Locate every Plasmodium parasite.
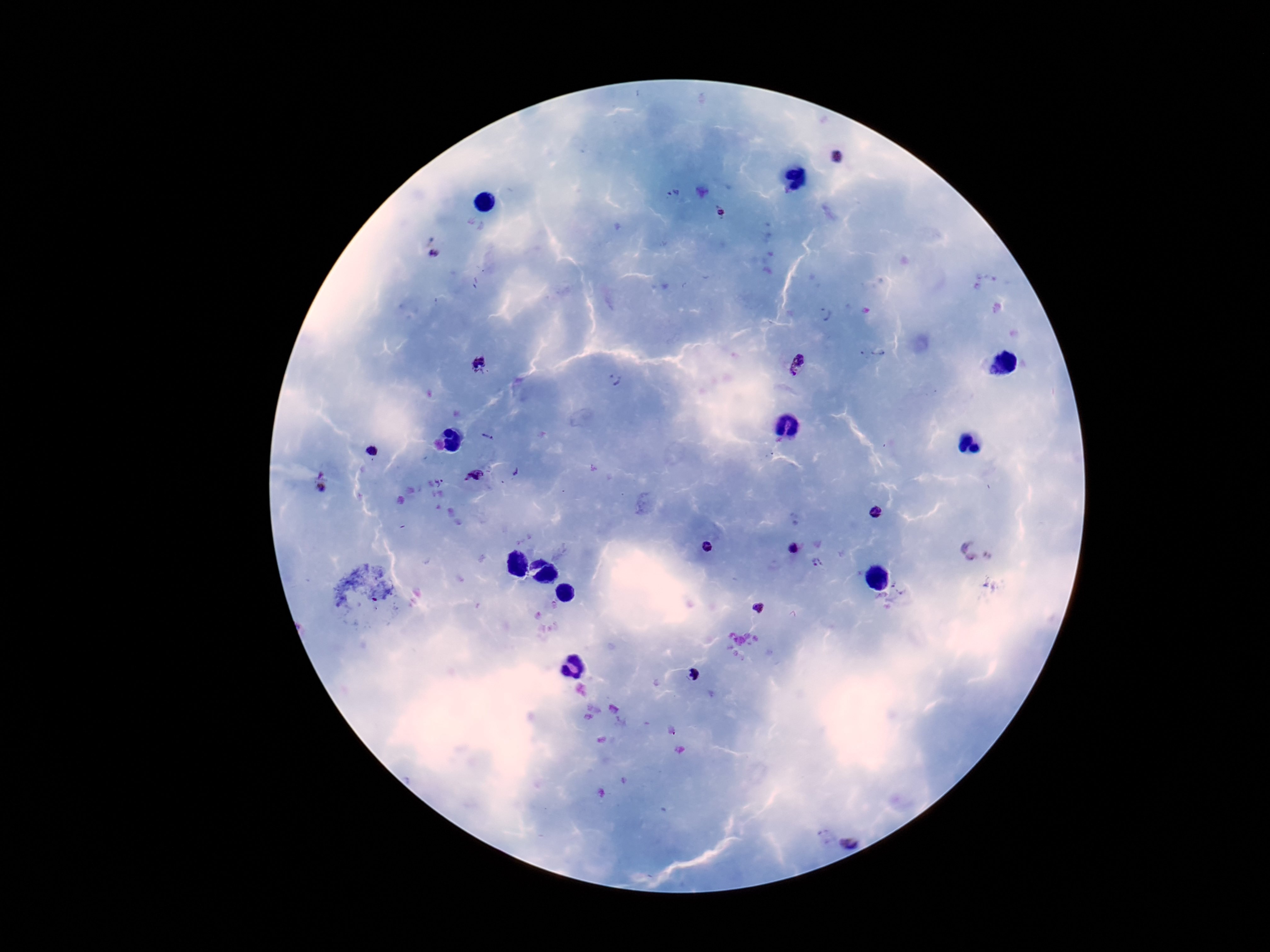

Approximate centers as [x, y] in pixels.
Plasmodium parasites: [837, 157], [674, 194], [722, 212], [434, 255], [827, 314], [873, 351], [799, 363], [481, 366], [614, 380], [487, 439], [372, 452], [515, 472], [323, 474], [474, 476], [441, 483], [322, 489], [876, 513], [708, 547], [794, 548], [969, 551], [817, 564], [759, 607], [693, 675], [850, 842].

Summary:
  - Image size: 1270×952 pixels
  - Capture: smartphone camera through the microscope eyepiece
  - Stain: Giemsa
  - Magnification: 100x
  - Field of view: single
  - Preparation: thick blood film
  - Patient malaria status: infected